State which cell type is depicted.
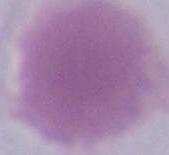

An erythrocyte.

{
  "modality": "micrograph",
  "magnification": "1000x"
}